Name the parasite shown.
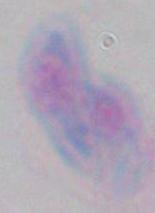

This is Toxoplasma gondii.

Captured at 1000x magnification. Micrograph.